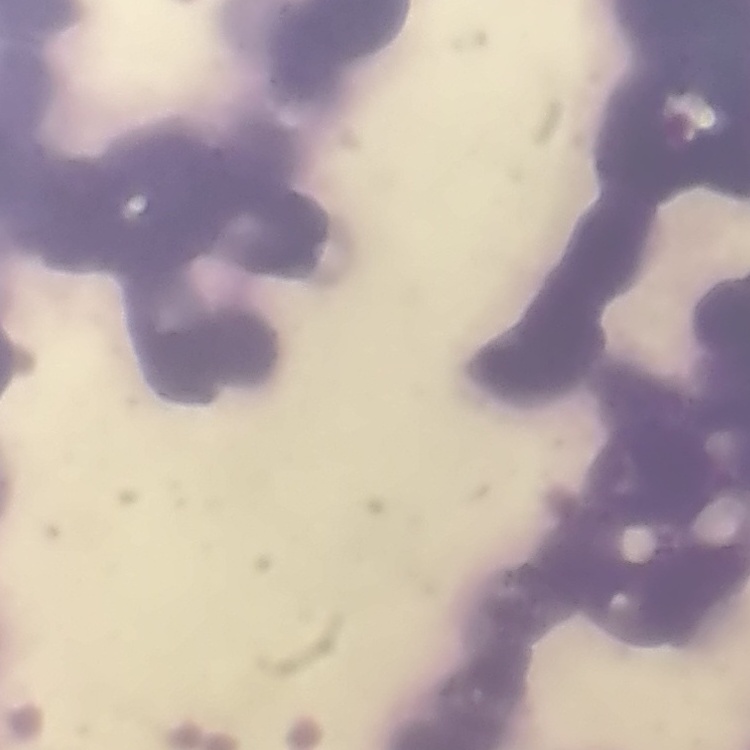

Summary:
  - Erythrocyte morphology: rouleaux formation
  - Preparation: thin peripheral smear
  - Stain: Field's or Giemsa
  - Image type: one tile cut from a larger photomicrograph